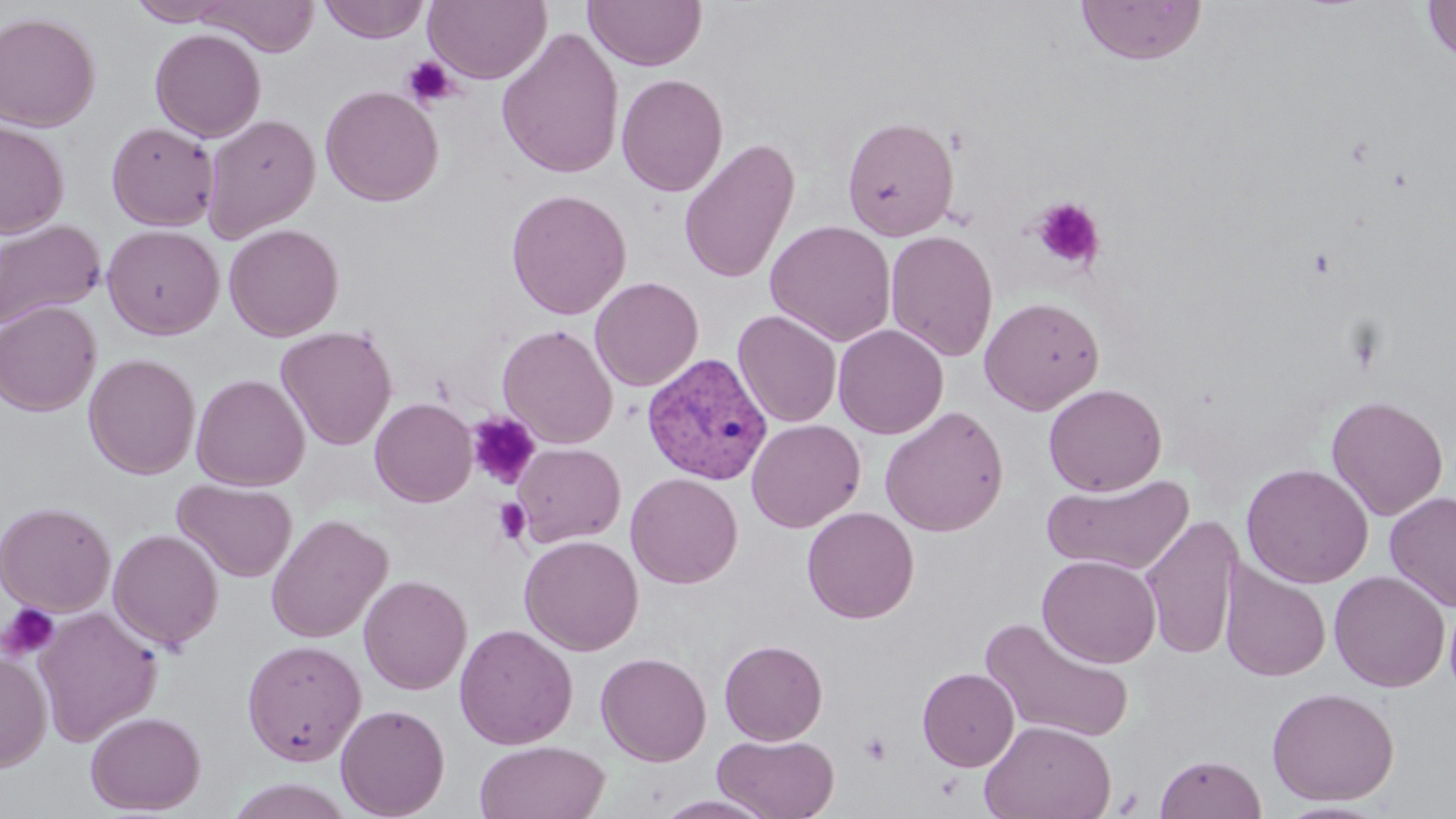
Approximate bounding boxes as (x1,y1)-(x2,y2) corner pairs in pixels. Platelet locations: (401,55)-(459,110), (1031,197)-(1105,271), (467,411)-(541,489), (493,498)-(531,545), (0,602)-(61,662), (859,733)-(892,765). Uninfected red blood cell locations: (126,0)-(239,26), (194,0)-(319,56), (319,0)-(429,43), (423,0)-(551,84), (582,0)-(707,72), (1077,0)-(1207,65), (1422,0)-(1456,63), (0,12)-(101,132), (496,27)-(625,180), (150,28)-(266,142), (616,72)-(729,197), (320,85)-(444,207), (202,113)-(320,242), (841,115)-(959,241), (0,120)-(69,238), (106,121)-(219,231), (678,137)-(799,284), (505,188)-(632,320), (0,218)-(106,331), (764,219)-(896,347), (224,223)-(344,341), (102,225)-(224,340), (885,230)-(999,362), (590,276)-(704,391), (979,296)-(1104,415), (0,300)-(102,416), (733,309)-(842,427), (498,323)-(618,448), (832,324)-(949,439), (275,325)-(398,450), (83,353)-(200,479), (191,373)-(310,490), (1043,383)-(1167,497), (1326,395)-(1449,521), (370,397)-(477,507), (879,406)-(1009,537), (746,419)-(865,533), (513,443)-(626,546), (1240,463)-(1374,588), (625,472)-(743,588), (1041,473)-(1195,576), (173,479)-(297,583), (1384,490)-(1456,613), (0,500)-(116,617), (802,506)-(919,624), (266,514)-(392,643), (0,515)-(222,626), (1140,516)-(1244,659), (107,529)-(224,650), (519,534)-(644,655), (1037,554)-(1161,667), (1220,562)-(1331,682), (1329,571)-(1450,692), (358,574)-(472,695), (34,606)-(162,746), (980,617)-(1135,744), (454,623)-(578,750), (719,639)-(828,745), (241,640)-(366,765), (0,650)-(52,772), (595,652)-(712,766), (917,667)-(1019,771), (1266,686)-(1399,806), (335,704)-(450,818), (85,710)-(206,815), (980,719)-(1116,819), (713,733)-(839,819), (474,740)-(609,819), (1155,753)-(1266,818), (654,793)-(778,818), (1277,800)-(1391,818). Plasmodium vivax-infected red blood cell locations: (642,353)-(772,485). Slide-level diagnosis: Plasmodium vivax. One field of a larger specimen. Optical microscopy. 1000x magnification. May-Grünwald-Giemsa stain. Image is 1456×819 pixels. Thin blood film.